Classify this cell by malaria status.
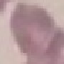
Uninfected.

Automatically extracted cell patch, resized to 64 × 64 pixels. Photographed with a smartphone camera at the microscope eyepiece. Thin blood smear. Giemsa-stained preparation.